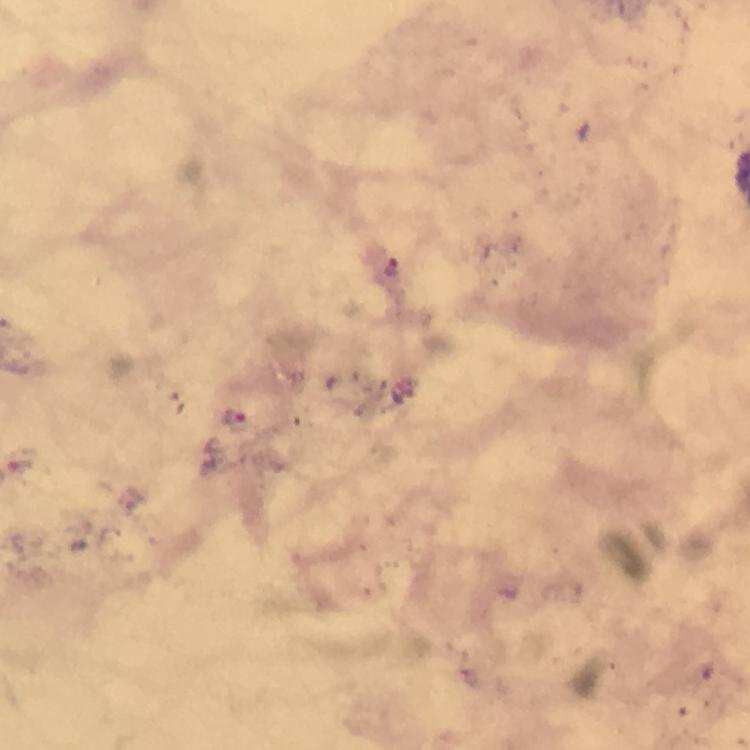 Approximate centers as [x, y] in pixels. Malaria parasite locations: [392, 267], [236, 417], [18, 458]. Giemsa stain. Thick smear. A crop from one field of view. Photographed with a smartphone mounted on the microscope. Immersion oil applied. From a malaria diagnostic workup. At 100x magnification. Image is 750×750 pixels.